Describe the morphology of the red blood cells.
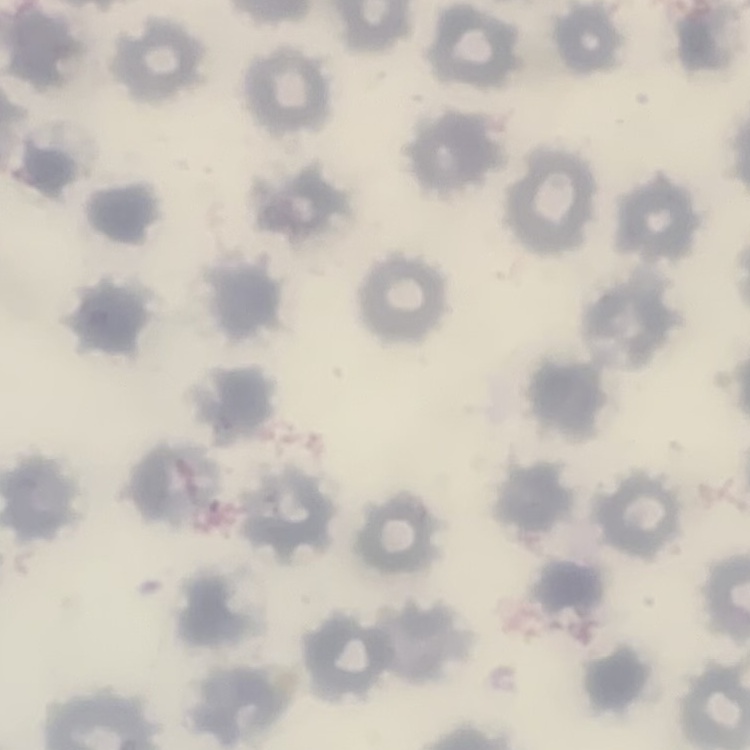

They show no rouleaux formation.

Stained with either Field's or Giemsa. Thin peripheral smear. One tile cut from a larger photomicrograph.